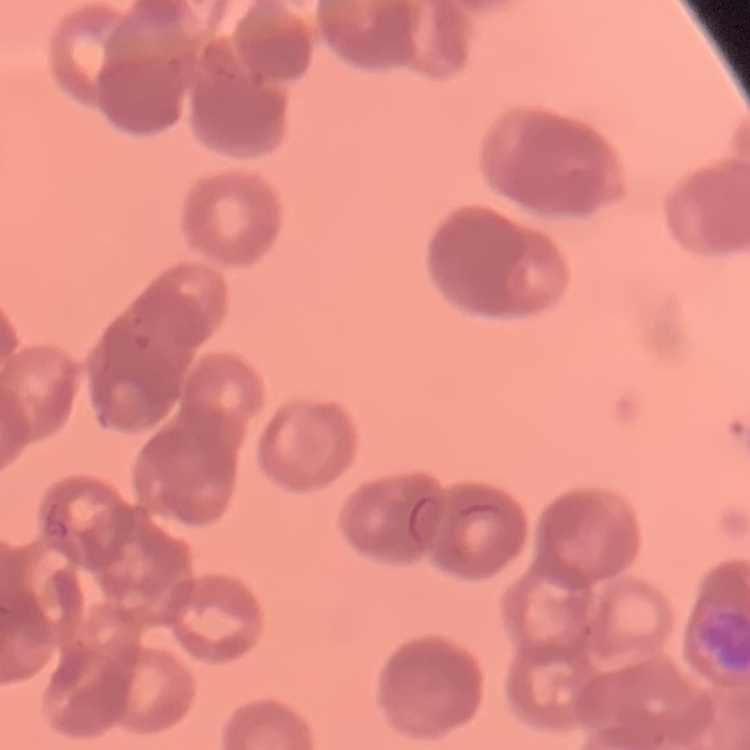
Summary:
  - Erythrocyte morphology: rouleaux formation
  - Preparation: thin blood smear
  - Stain: Field's or Giemsa
  - Image type: square crop of a larger photomicrograph